Assess the morphology of the red blood cells.
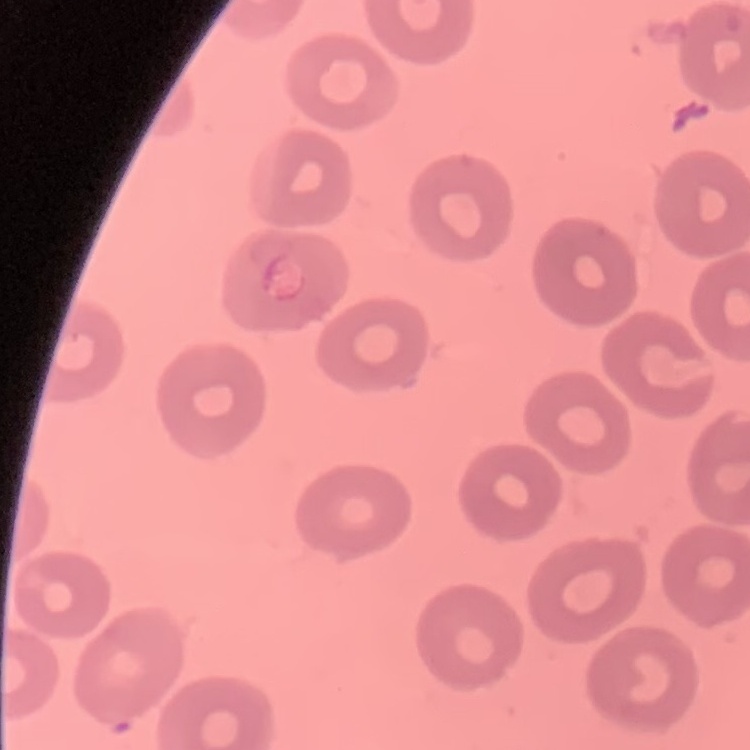
They show no rouleaux formation.

Square crop of a larger photomicrograph. Stained with either Field's or Giemsa. Thin blood smear.